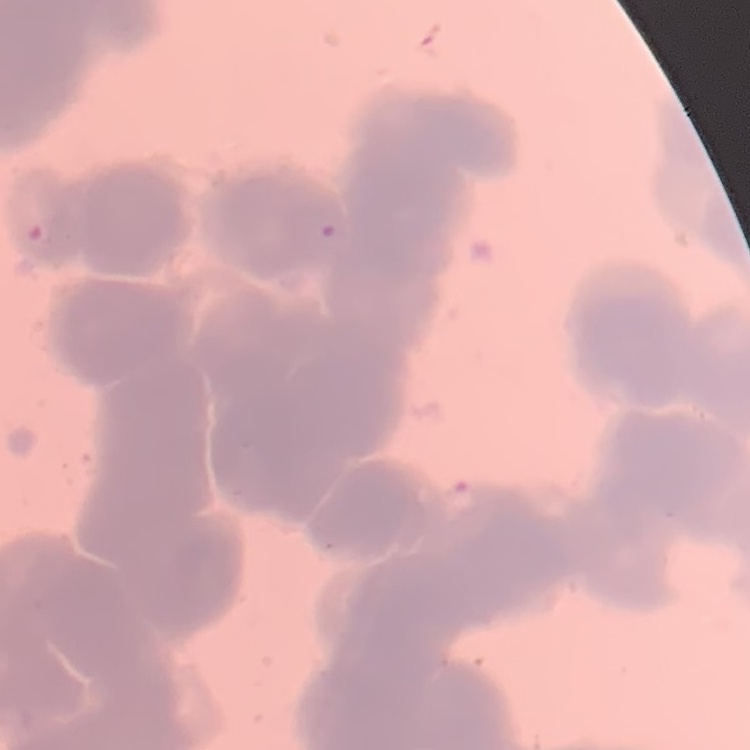

Summary:
  - Erythrocyte morphology: rouleaux formation
  - Stain: Field's or Giemsa
  - Image type: one tile cut from a larger photomicrograph
  - Preparation: thin peripheral smear